Locate every uninfected red blood cell.
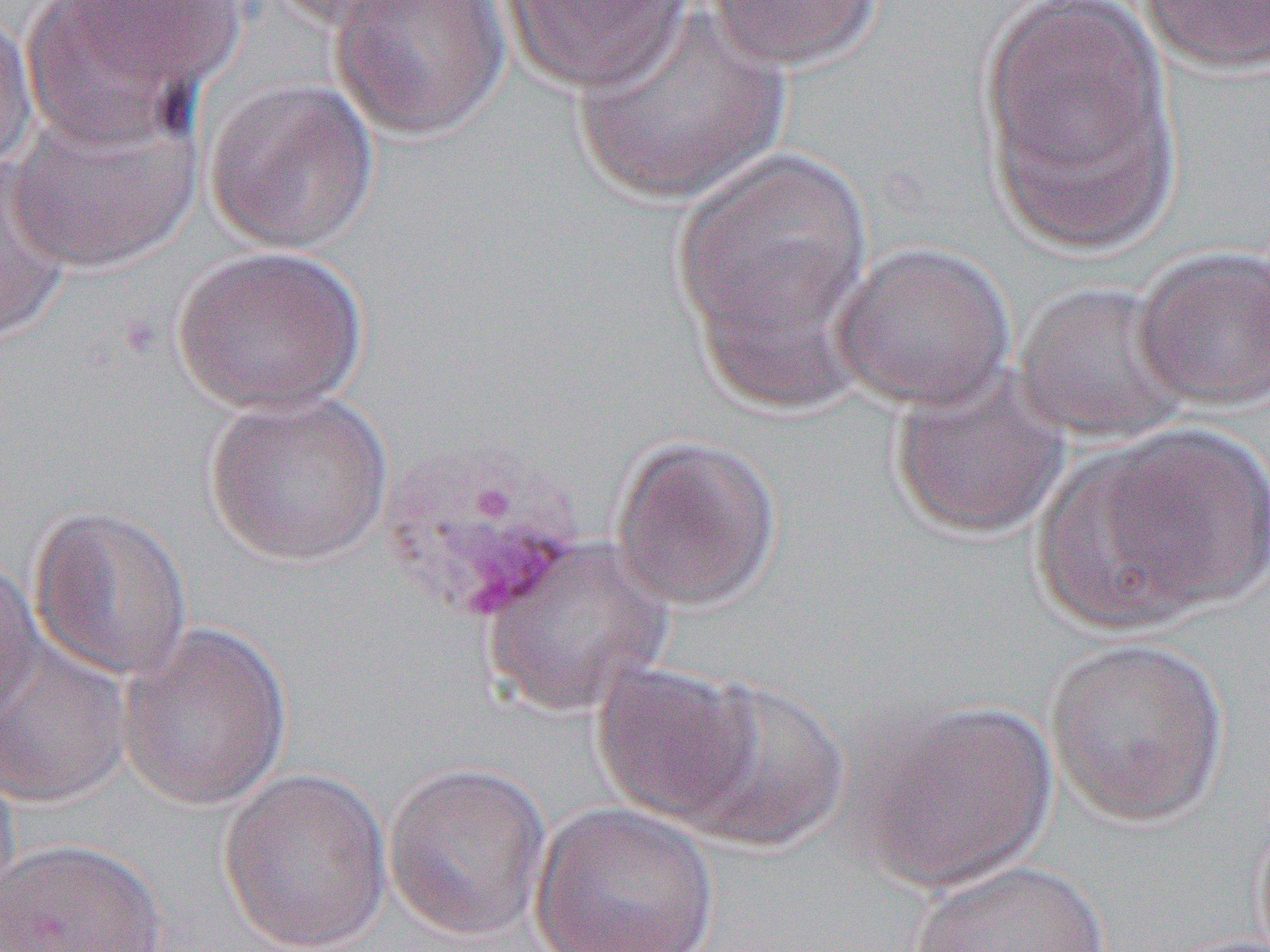

Approximate bounding boxes as (x1,y1)-(x2,y2) corner pairs in pixels.
Uninfected red blood cells: (55,0)-(247,87), (259,0)-(427,30), (330,0)-(510,141), (501,0)-(695,94), (701,0)-(887,71), (1136,0)-(1270,77), (979,2)-(1182,249), (19,4)-(225,147), (572,7)-(790,206), (0,9)-(37,177), (202,77)-(379,255), (8,96)-(204,275), (672,145)-(877,388), (0,156)-(72,344), (831,242)-(1017,414), (170,246)-(368,416), (1132,246)-(1270,413), (1011,280)-(1198,447), (887,375)-(1070,541), (201,390)-(394,567), (1052,424)-(1269,625), (607,433)-(783,614), (28,505)-(193,684), (478,536)-(674,716), (0,560)-(42,734), (116,620)-(293,813), (1,637)-(133,811), (1044,637)-(1230,828), (590,660)-(762,829), (668,676)-(850,855), (855,700)-(1058,890), (0,755)-(22,918), (383,760)-(552,941), (218,767)-(392,951), (1248,792)-(1270,952), (529,802)-(720,952), (0,838)-(169,951), (909,860)-(1112,952).

slide-level diagnosis = Plasmodium vivax
magnification = 1000x
field of view = one of a larger specimen
preparation = thin blood film
modality = light microscopy
image size = 1270×952 pixels